Describe the morphology of the red blood cells.
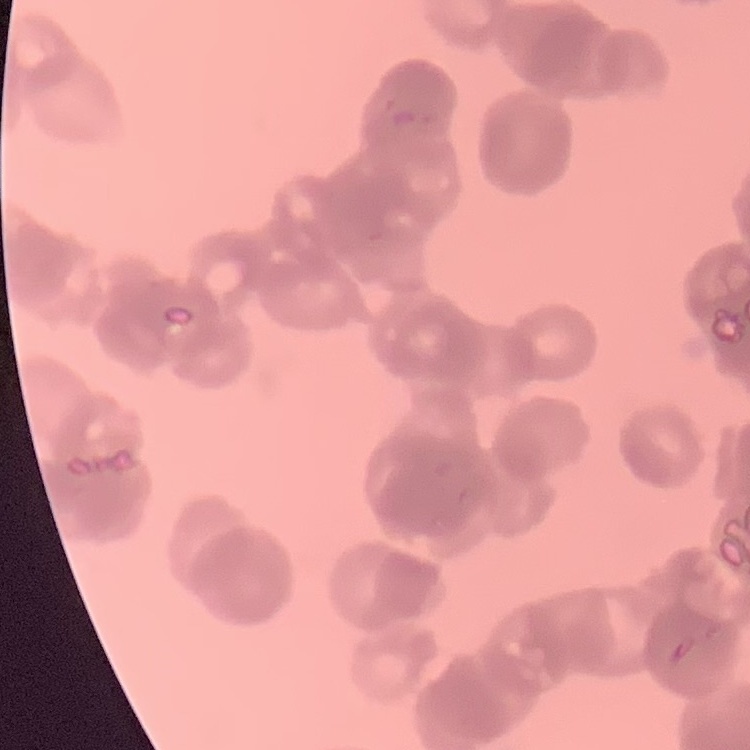

They show rouleaux formation.

Thin peripheral smear. One tile cut from a larger photomicrograph. Field's or Giemsa stain.